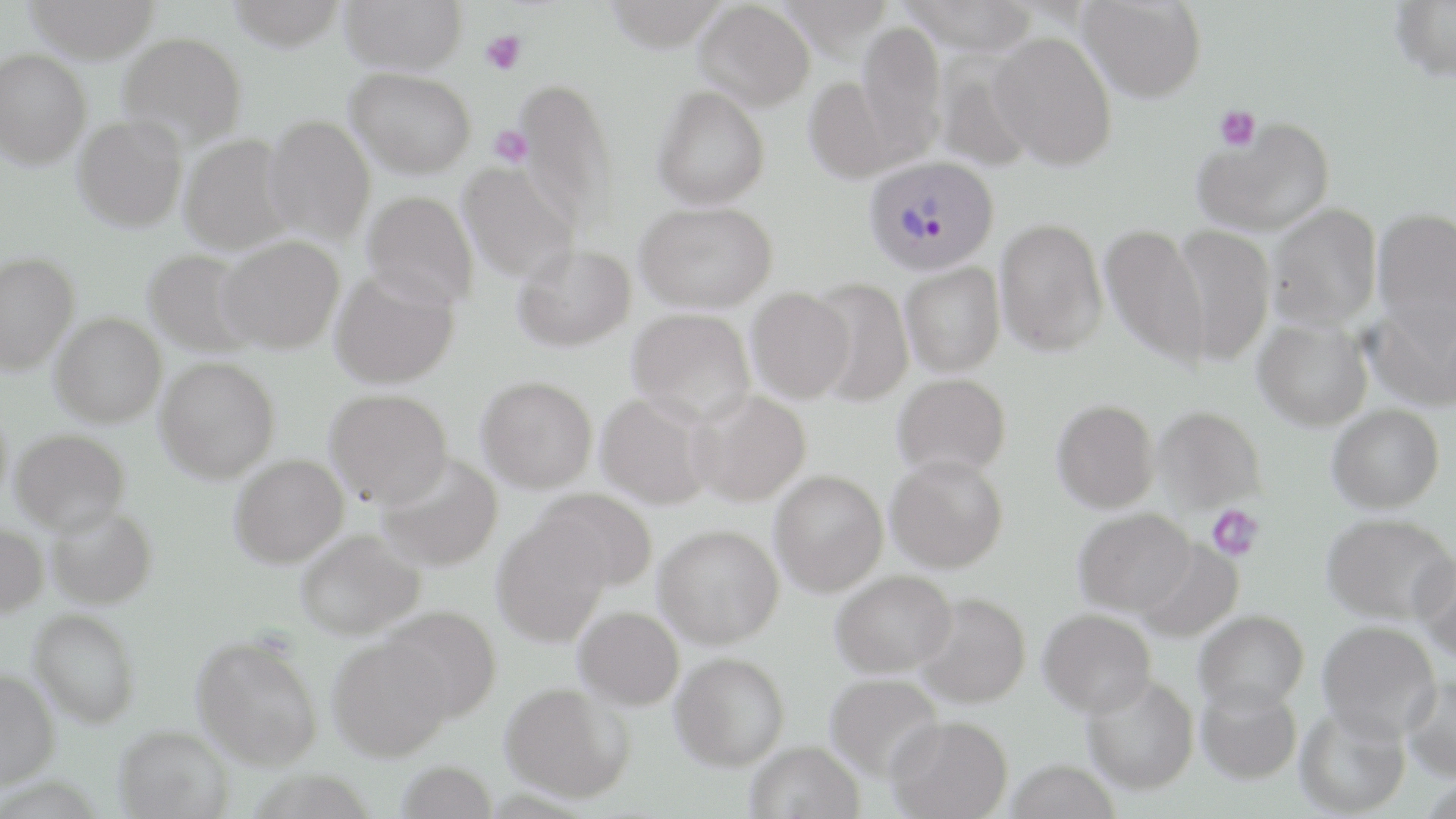
{
  "slide_level_diagnosis": "Plasmodium vivax",
  "field_of_view": "single",
  "platelet_locations": "approximate bounding boxes as (x1, y1, x2, y2) in pixels: (480, 30, 526, 75), (1215, 104, 1260, 151), (488, 124, 532, 167), (1206, 505, 1264, 561)",
  "plasmodium_vivax_infected_red_blood_cell_locations": "approximate bounding boxes as (x1, y1, x2, y2) in pixels: (864, 155, 999, 275)",
  "uninfected_red_blood_cell_locations": "approximate bounding boxes as (x1, y1, x2, y2) in pixels: (25, 0, 159, 63), (227, 0, 348, 50), (340, 0, 467, 74), (604, 0, 730, 50), (695, 0, 815, 109), (899, 0, 1041, 55), (1079, 0, 1206, 103), (1390, 0, 1456, 81), (855, 21, 947, 160), (118, 31, 247, 149), (990, 31, 1117, 169), (0, 50, 92, 169), (934, 51, 1036, 171), (347, 68, 477, 178), (804, 76, 903, 181), (514, 77, 620, 232), (653, 84, 770, 209), (73, 114, 187, 232), (264, 115, 376, 243), (1193, 117, 1335, 238), (180, 134, 295, 254), (457, 161, 580, 283), (363, 191, 479, 309), (636, 201, 777, 311), (1268, 204, 1381, 331), (1372, 208, 1456, 334), (995, 218, 1107, 355), (1100, 224, 1211, 368), (1172, 224, 1275, 365), (218, 236, 345, 353), (513, 243, 635, 351), (143, 249, 262, 357), (0, 252, 79, 375), (900, 262, 1005, 376), (330, 270, 459, 389), (807, 278, 913, 405), (746, 287, 855, 403), (1363, 303, 1456, 415), (627, 307, 756, 423), (50, 312, 166, 426), (1254, 318, 1373, 431), (155, 357, 280, 482), (893, 373, 1011, 479), (477, 376, 598, 492), (325, 389, 453, 506), (688, 390, 811, 506), (595, 392, 715, 509), (1052, 399, 1159, 513), (1328, 404, 1445, 513), (1153, 406, 1266, 511), (10, 429, 130, 533), (377, 453, 503, 571), (229, 454, 348, 567), (886, 454, 1008, 572), (770, 470, 888, 596), (534, 488, 657, 593), (46, 505, 157, 608), (1074, 508, 1195, 616), (1321, 512, 1456, 624), (492, 517, 610, 646), (0, 523, 48, 619), (654, 524, 784, 647), (296, 530, 424, 639), (1134, 539, 1244, 642), (1413, 548, 1456, 661), (831, 569, 957, 677), (915, 592, 1031, 708), (379, 606, 502, 722), (574, 606, 684, 709), (1039, 608, 1157, 717), (30, 609, 141, 727), (1194, 610, 1309, 712), (1318, 620, 1441, 740), (191, 634, 323, 770), (328, 635, 456, 760), (670, 652, 790, 770), (0, 669, 60, 789), (826, 673, 944, 780), (1402, 673, 1456, 780), (1083, 674, 1199, 794), (1196, 681, 1303, 783), (501, 682, 634, 802), (1295, 705, 1410, 817), (885, 715, 1013, 819), (114, 725, 233, 818), (745, 741, 864, 819), (1006, 759, 1120, 819), (396, 760, 497, 818)",
  "magnification": "1000x",
  "preparation": "thin blood film",
  "image_size": "1456×819 pixels",
  "stain": "May-Grünwald-Giemsa",
  "modality": "optical microscopy"
}